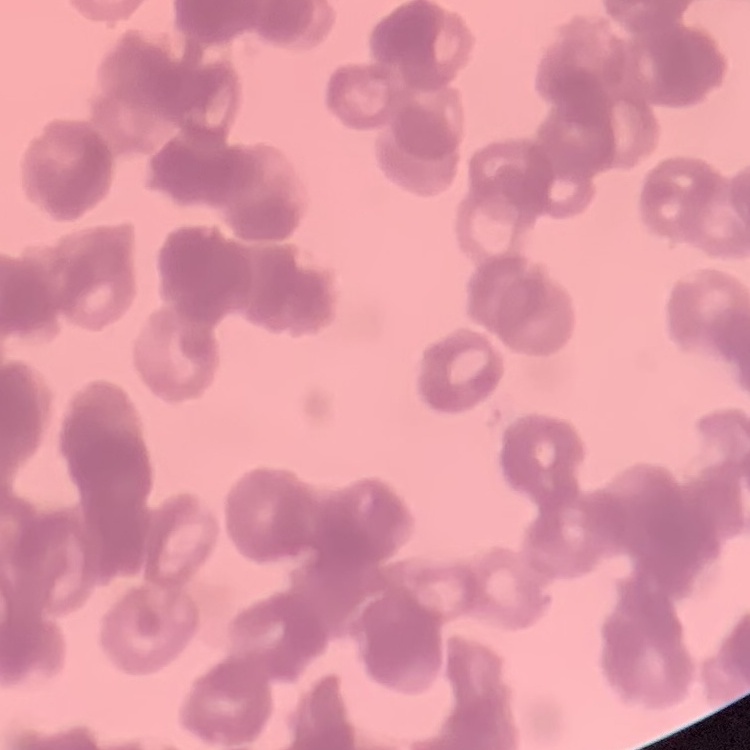
red blood cell morphology = rouleaux formation
stain = Field's or Giemsa
image type = one tile cut from a larger photomicrograph
preparation = thin peripheral smear